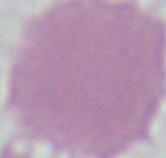

identification = erythrocyte
modality = photomicrograph
magnification = 1000x